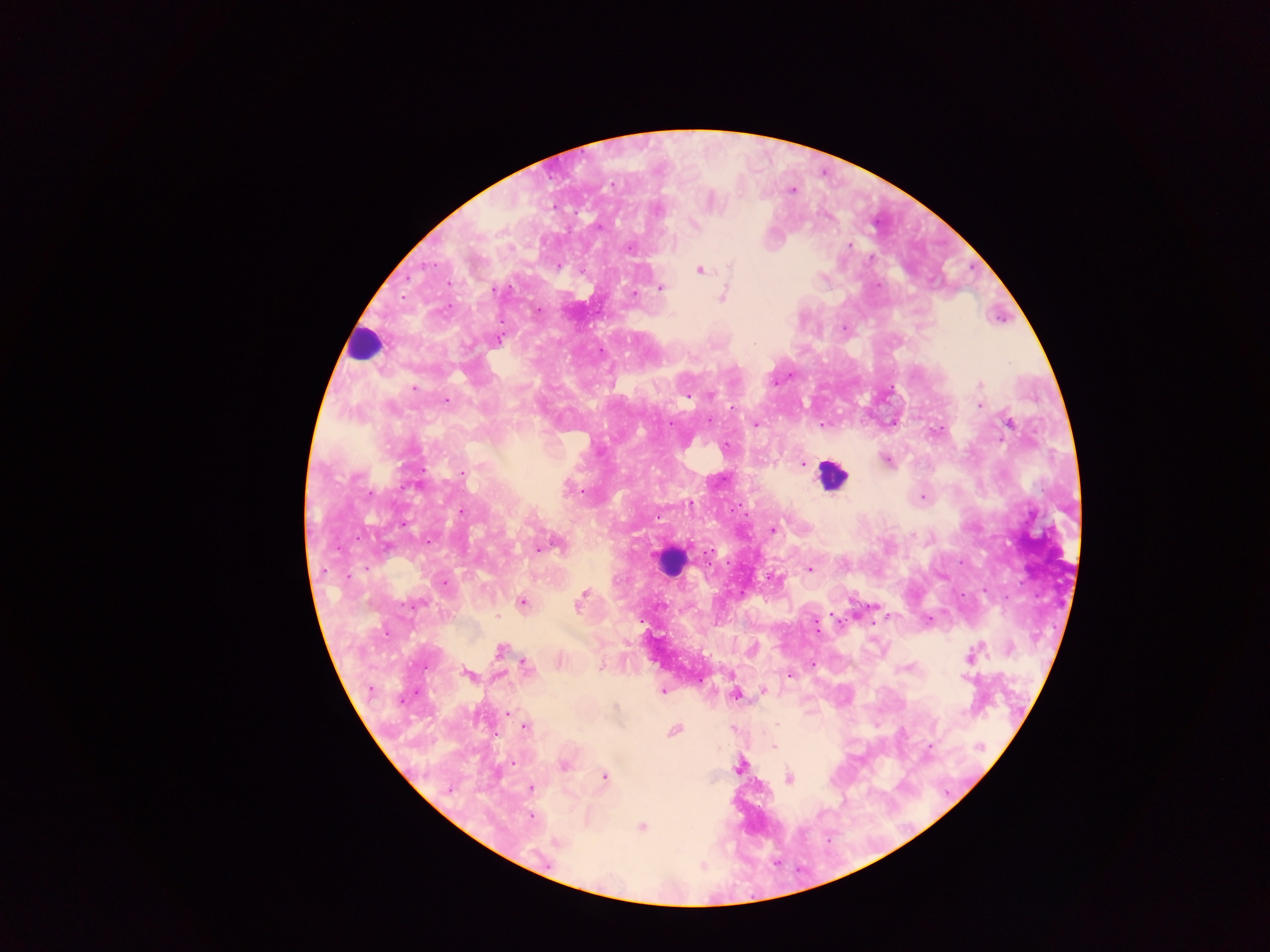

Approximate centers as (x, y) in pixels. Plasmodium parasite locations: (612, 183), (791, 190), (658, 211), (695, 225), (849, 246), (628, 247), (730, 267), (583, 271), (700, 271), (661, 288), (495, 290), (634, 294), (721, 298), (538, 310), (499, 340), (754, 343), (600, 350), (980, 384), (414, 389), (711, 395), (687, 396), (447, 401), (979, 405), (709, 421), (1009, 423), (756, 425), (822, 425), (726, 448), (886, 460), (803, 464), (462, 473), (413, 486), (582, 491), (922, 497), (691, 504), (461, 513), (772, 529), (427, 540), (558, 544), (539, 548), (809, 569), (349, 577), (444, 584), (583, 593), (581, 600), (523, 603), (412, 604), (497, 617), (928, 619), (500, 650), (973, 653), (812, 664), (526, 667), (599, 667), (467, 673), (790, 676), (963, 677), (370, 689), (663, 691), (763, 691), (736, 696), (402, 700), (615, 706), (508, 713), (777, 725), (524, 727), (675, 731), (930, 746), (774, 747), (981, 747), (513, 762), (563, 765), (740, 767), (604, 776), (789, 779), (531, 788), (531, 818), (641, 827), (557, 843). Leukocyte locations: (364, 344), (832, 474), (670, 561). Collected in Ghana. Image is 1270×952 pixels. Photographed through a microscope with a mobile-phone camera. One field of view. Thick blood smear.